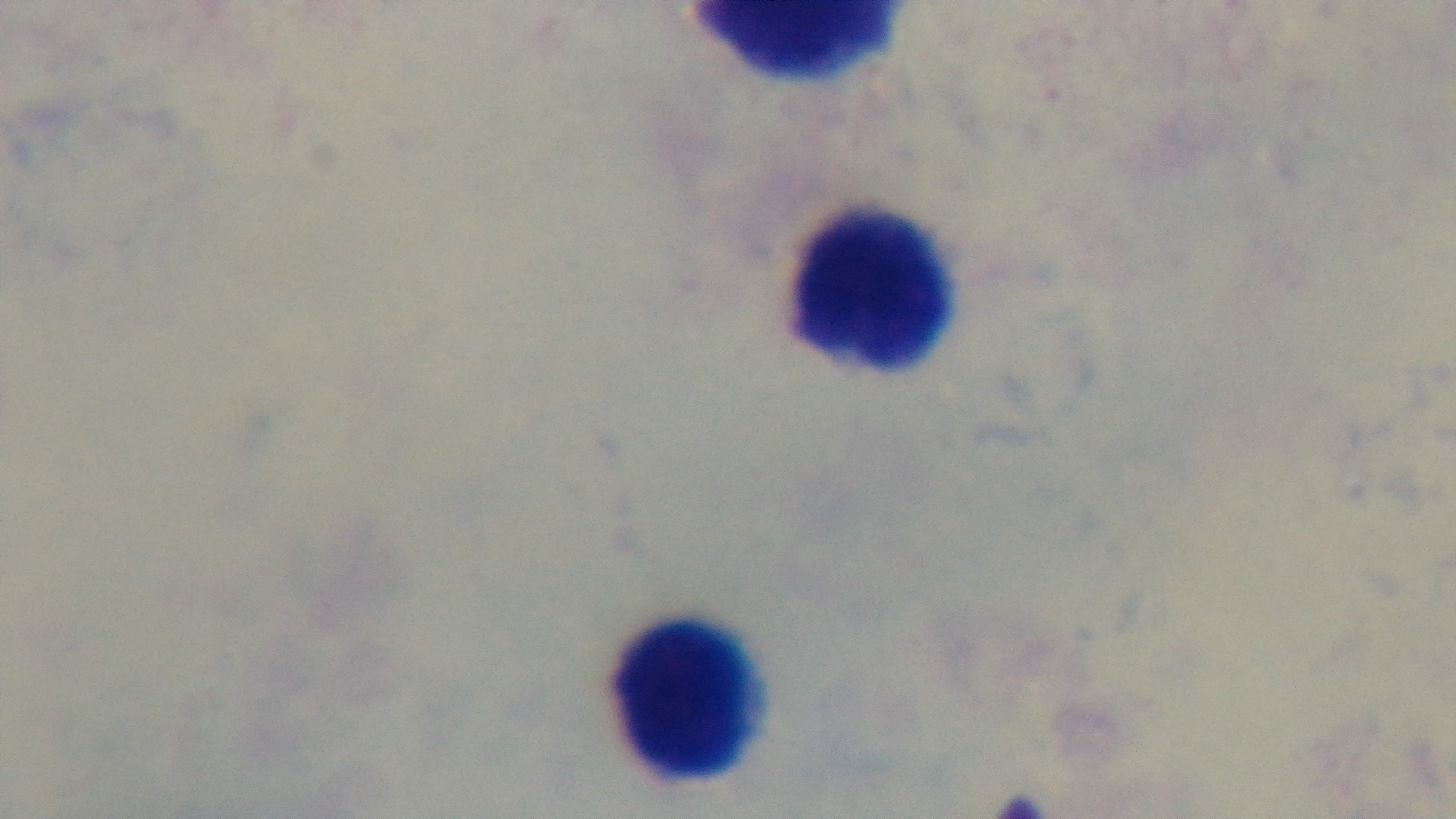
Summary:
  - Stain: Giemsa
  - Preparation: thick blood film
  - Field of view: single
  - Objective: 100x oil immersion
  - Capture: mounted 4K digital camera
  - Modality: light microscopy
  - Malaria status: negative